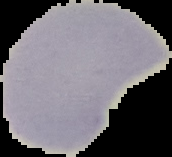
Summary:
  - Image size: 172×157 pixels
  - Result: negative for Plasmodium parasites
  - Preparation: thin blood smear
  - Image type: cell region segmented out of the field of view; surrounding area masked to black